Classify this cell by malaria status.
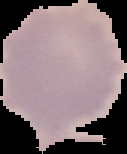
Uninfected.

Summary:
  - Image size: 127×154 pixels
  - Preparation: thin blood film
  - Image type: cell region segmented out of the field of view; surrounding area masked to black